Outline each blood parasite and name the species.
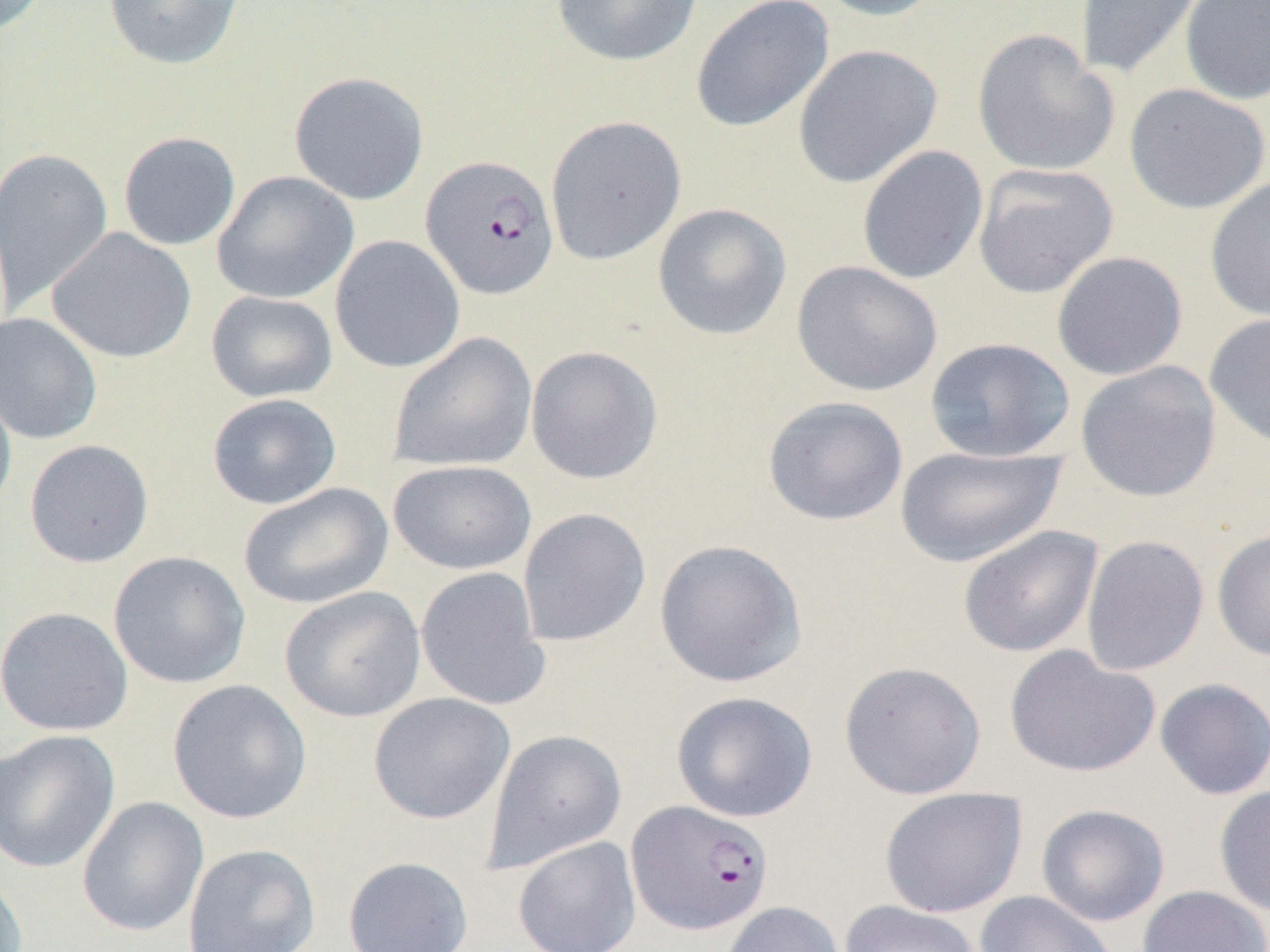

Approximate bounding boxes as named x1/y1/x2/y2 corners in pixels.
Plasmodium falciparum-infected red blood cells: (x1=420, y1=154, x2=559, y2=300), (x1=626, y1=800, x2=773, y2=935).
No Plasmodium ovale, Plasmodium malariae, Plasmodium vivax, Babesia divergens, or Trypanosoma brucei observed.

Summary:
  - Uninfected red blood cell locations: (x1=0, y1=0, x2=49, y2=36), (x1=102, y1=0, x2=245, y2=70), (x1=551, y1=0, x2=703, y2=67), (x1=810, y1=0, x2=948, y2=22), (x1=1075, y1=0, x2=1208, y2=81), (x1=1179, y1=0, x2=1270, y2=106), (x1=690, y1=1, x2=835, y2=133), (x1=972, y1=29, x2=1120, y2=177), (x1=792, y1=43, x2=942, y2=188), (x1=288, y1=71, x2=430, y2=206), (x1=1123, y1=83, x2=1269, y2=214), (x1=544, y1=115, x2=687, y2=265), (x1=118, y1=132, x2=241, y2=251), (x1=1, y1=145, x2=114, y2=315), (x1=857, y1=145, x2=988, y2=285), (x1=972, y1=163, x2=1119, y2=299), (x1=211, y1=171, x2=358, y2=304), (x1=1204, y1=177, x2=1270, y2=322), (x1=652, y1=202, x2=792, y2=341), (x1=46, y1=227, x2=197, y2=364), (x1=330, y1=235, x2=465, y2=374), (x1=1051, y1=251, x2=1188, y2=381), (x1=791, y1=261, x2=943, y2=397), (x1=206, y1=290, x2=338, y2=403), (x1=0, y1=312, x2=102, y2=445), (x1=1203, y1=312, x2=1270, y2=449), (x1=388, y1=332, x2=537, y2=473), (x1=924, y1=336, x2=1076, y2=463), (x1=525, y1=345, x2=664, y2=485), (x1=1075, y1=360, x2=1222, y2=502), (x1=0, y1=377, x2=18, y2=523), (x1=207, y1=393, x2=342, y2=509), (x1=762, y1=395, x2=908, y2=526), (x1=24, y1=439, x2=154, y2=568), (x1=894, y1=444, x2=1067, y2=568), (x1=388, y1=460, x2=537, y2=575), (x1=239, y1=482, x2=394, y2=609), (x1=517, y1=507, x2=651, y2=647), (x1=957, y1=525, x2=1103, y2=658), (x1=1212, y1=527, x2=1270, y2=661), (x1=1080, y1=534, x2=1210, y2=676), (x1=653, y1=538, x2=808, y2=688), (x1=107, y1=551, x2=251, y2=689), (x1=415, y1=567, x2=550, y2=711), (x1=280, y1=586, x2=427, y2=723), (x1=0, y1=606, x2=134, y2=737), (x1=1004, y1=644, x2=1161, y2=779), (x1=839, y1=660, x2=987, y2=800), (x1=167, y1=678, x2=312, y2=824), (x1=1154, y1=678, x2=1270, y2=801), (x1=368, y1=691, x2=515, y2=825), (x1=670, y1=691, x2=819, y2=823), (x1=481, y1=728, x2=627, y2=874), (x1=0, y1=729, x2=121, y2=874), (x1=1213, y1=783, x2=1270, y2=917), (x1=879, y1=786, x2=1028, y2=919), (x1=77, y1=796, x2=209, y2=937), (x1=1036, y1=804, x2=1170, y2=926), (x1=512, y1=836, x2=641, y2=952), (x1=182, y1=843, x2=320, y2=952), (x1=342, y1=856, x2=474, y2=952), (x1=0, y1=869, x2=28, y2=952), (x1=1137, y1=885, x2=1269, y2=952), (x1=975, y1=890, x2=1117, y2=952), (x1=839, y1=900, x2=983, y2=952), (x1=719, y1=901, x2=846, y2=952)
  - Slide-level diagnosis: Plasmodium falciparum
  - Modality: optical microscopy
  - Preparation: thin blood film
  - Magnification: 1000x
  - Image size: 1270×952 pixels
  - Field of view: one of a larger specimen